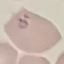
Summary:
  - Malaria status: parasitized
  - Image type: automatically extracted cell patch, resized to 64 × 64 pixels
  - Stain: Giemsa
  - Preparation: thin smear
  - Capture: smartphone camera at the microscope eyepiece